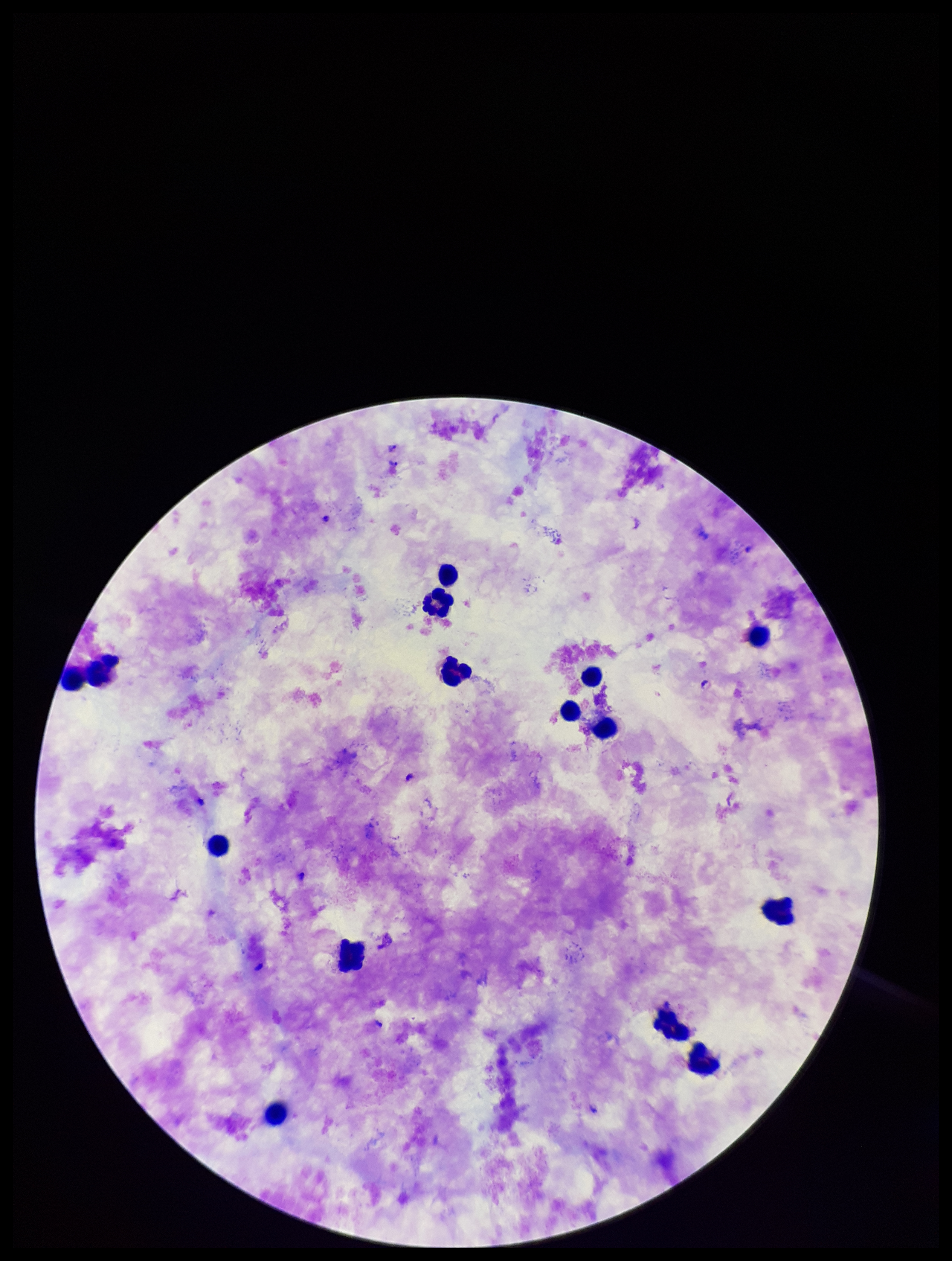

Summary:
  - Leukocyte count: 14
  - Field of view: one from this slide
  - Stain: Giemsa
  - Patient malaria status: infected
  - Capture: smartphone photograph through the microscope eyepiece
  - Image size: 952×1261 pixels
  - Parasite count: 2
  - Species reported for this patient: Plasmodium falciparum
  - Preparation: thick blood smear
  - Plasmodium parasites: detected